Classify this cell by malaria status.
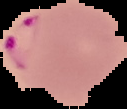

It is parasitized.

Summary:
  - Image type: cell region segmented out of the field of view; surrounding area masked to black
  - Preparation: thin blood smear
  - Image size: 127×109 pixels